Name the blood parasite species.
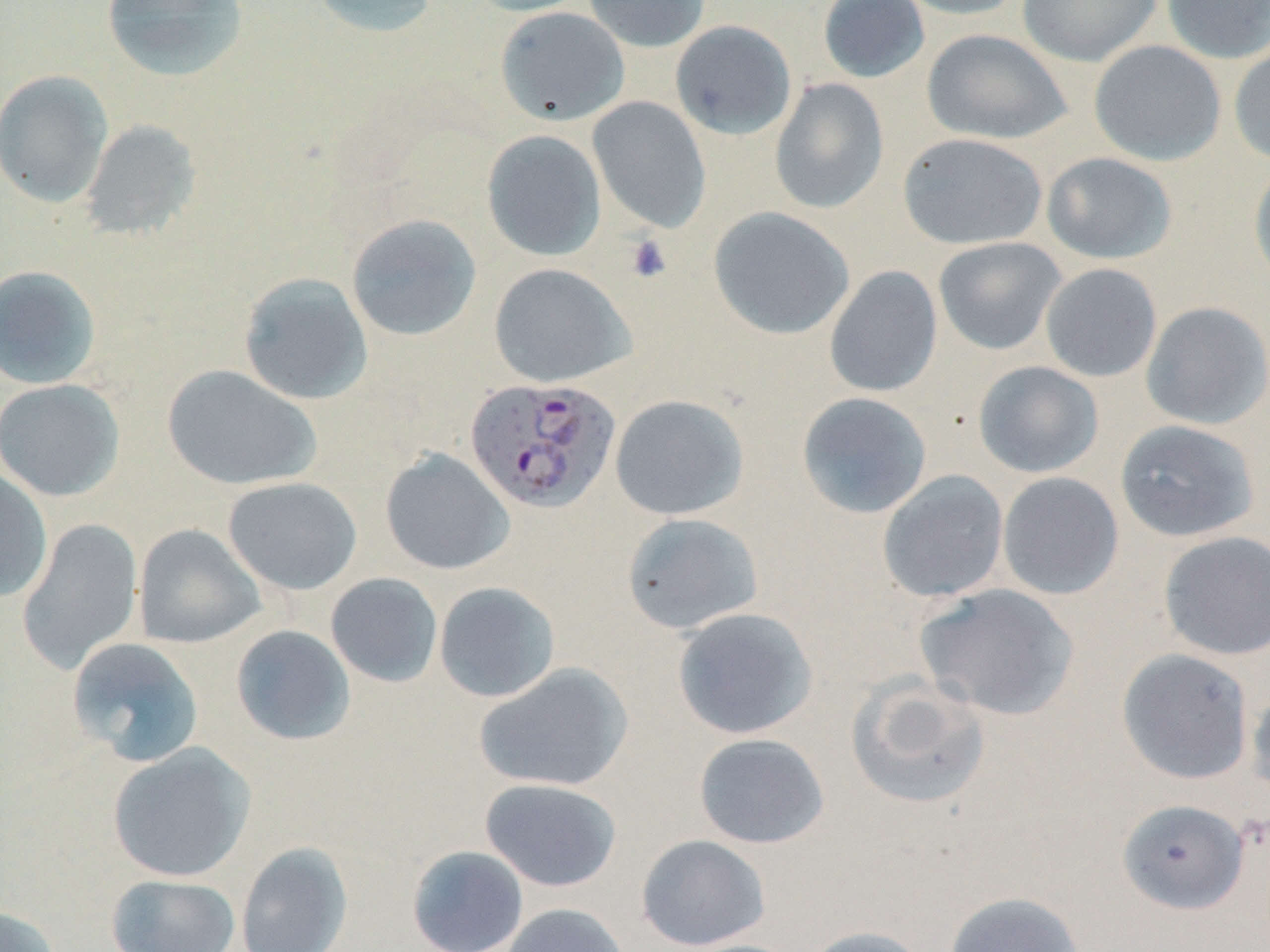
Plasmodium falciparum.

Approximate bounding boxes as named x1/y1/x2/y2 corners in pixels. Plasmodium falciparum-infected red blood cell locations: (x1=465, y1=377, x2=621, y2=513). Uninfected red blood cell locations: (x1=101, y1=0, x2=249, y2=82), (x1=308, y1=0, x2=441, y2=38), (x1=465, y1=0, x2=593, y2=17), (x1=583, y1=0, x2=711, y2=53), (x1=817, y1=0, x2=930, y2=84), (x1=892, y1=0, x2=1029, y2=20), (x1=1017, y1=0, x2=1164, y2=67), (x1=1160, y1=0, x2=1270, y2=63), (x1=495, y1=7, x2=630, y2=126), (x1=670, y1=20, x2=797, y2=140), (x1=921, y1=29, x2=1072, y2=145), (x1=1088, y1=40, x2=1226, y2=166), (x1=1229, y1=42, x2=1270, y2=166), (x1=0, y1=70, x2=114, y2=207), (x1=770, y1=77, x2=889, y2=214), (x1=588, y1=96, x2=711, y2=233), (x1=80, y1=119, x2=201, y2=240), (x1=481, y1=130, x2=607, y2=261), (x1=898, y1=133, x2=1047, y2=250), (x1=1041, y1=151, x2=1177, y2=265), (x1=1248, y1=159, x2=1270, y2=288), (x1=708, y1=207, x2=855, y2=340), (x1=346, y1=213, x2=482, y2=342), (x1=933, y1=237, x2=1067, y2=356), (x1=488, y1=262, x2=635, y2=388), (x1=1040, y1=263, x2=1162, y2=382), (x1=0, y1=265, x2=102, y2=390), (x1=824, y1=265, x2=943, y2=397), (x1=238, y1=273, x2=373, y2=405), (x1=1140, y1=301, x2=1270, y2=430), (x1=972, y1=361, x2=1104, y2=478), (x1=162, y1=364, x2=321, y2=491), (x1=0, y1=379, x2=125, y2=502), (x1=796, y1=392, x2=932, y2=519), (x1=610, y1=394, x2=749, y2=521), (x1=1114, y1=419, x2=1260, y2=542), (x1=380, y1=449, x2=515, y2=575), (x1=0, y1=467, x2=53, y2=603), (x1=877, y1=470, x2=1009, y2=603), (x1=997, y1=472, x2=1124, y2=600), (x1=222, y1=477, x2=362, y2=595), (x1=621, y1=513, x2=764, y2=634), (x1=16, y1=517, x2=144, y2=675), (x1=133, y1=524, x2=267, y2=649), (x1=1158, y1=530, x2=1270, y2=661), (x1=325, y1=573, x2=443, y2=687), (x1=434, y1=582, x2=561, y2=702), (x1=914, y1=583, x2=1080, y2=721), (x1=671, y1=607, x2=818, y2=740), (x1=230, y1=624, x2=355, y2=746), (x1=66, y1=637, x2=205, y2=767), (x1=1116, y1=648, x2=1255, y2=785), (x1=474, y1=663, x2=633, y2=792), (x1=845, y1=673, x2=991, y2=810), (x1=1246, y1=682, x2=1270, y2=801), (x1=693, y1=733, x2=830, y2=849), (x1=107, y1=742, x2=256, y2=883), (x1=479, y1=778, x2=622, y2=892), (x1=1116, y1=799, x2=1250, y2=915), (x1=635, y1=833, x2=771, y2=951), (x1=235, y1=841, x2=354, y2=952), (x1=406, y1=845, x2=529, y2=952), (x1=105, y1=873, x2=241, y2=952), (x1=944, y1=890, x2=1085, y2=952), (x1=500, y1=902, x2=630, y2=952), (x1=0, y1=904, x2=63, y2=952), (x1=800, y1=925, x2=929, y2=952). Platelet locations: (x1=624, y1=234, x2=673, y2=284). Light microscopy. Captured at 1000x magnification. Image is 1270×952 pixels. May-Grünwald-Giemsa-stained preparation. One field of a larger specimen. Thin blood smear.